Give the position of every Plasmodium parasite visible.
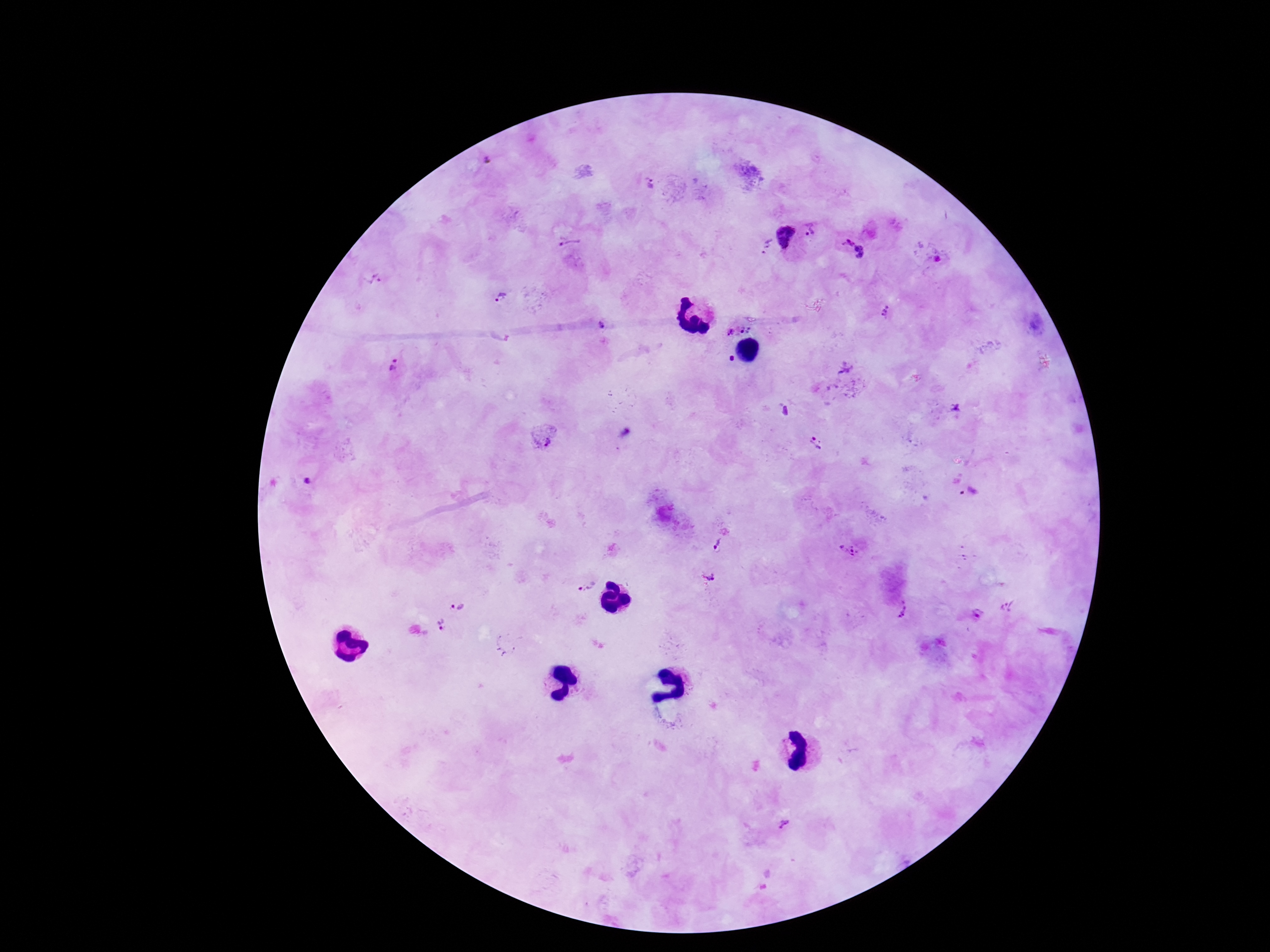

Approximate centers as {x, y} in pixels.
Plasmodium parasites: {489, 161}, {652, 182}, {811, 229}, {786, 235}, {572, 243}, {763, 246}, {852, 249}, {375, 277}, {501, 299}, {885, 311}, {607, 324}, {728, 330}, {397, 364}, {847, 367}, {955, 408}, {541, 438}, {818, 444}, {309, 482}, {721, 543}, {850, 549}, {707, 577}, {586, 586}, {458, 604}, {1010, 605}, {902, 610}, {978, 614}, {441, 624}, {786, 822}.

Giemsa stain. Smartphone photograph taken through the microscope eyepiece. Single field of view. Patient malaria status: infected. Thick blood smear. Image is 1270×952 pixels. 100x magnification.